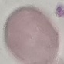

Malaria status: uninfected. Thin blood film. Acquired by smartphone through the microscope eyepiece. Giemsa-stained preparation. Cell patch, automatically extracted from a larger field of view and resized to 64 × 64 pixels.